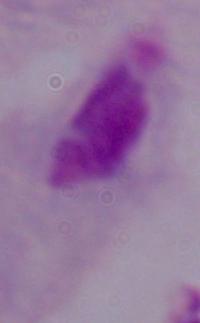
Summary:
  - Magnification: 1000x
  - Modality: photomicrograph
  - Identification: trichomonad